State the blood parasite species.
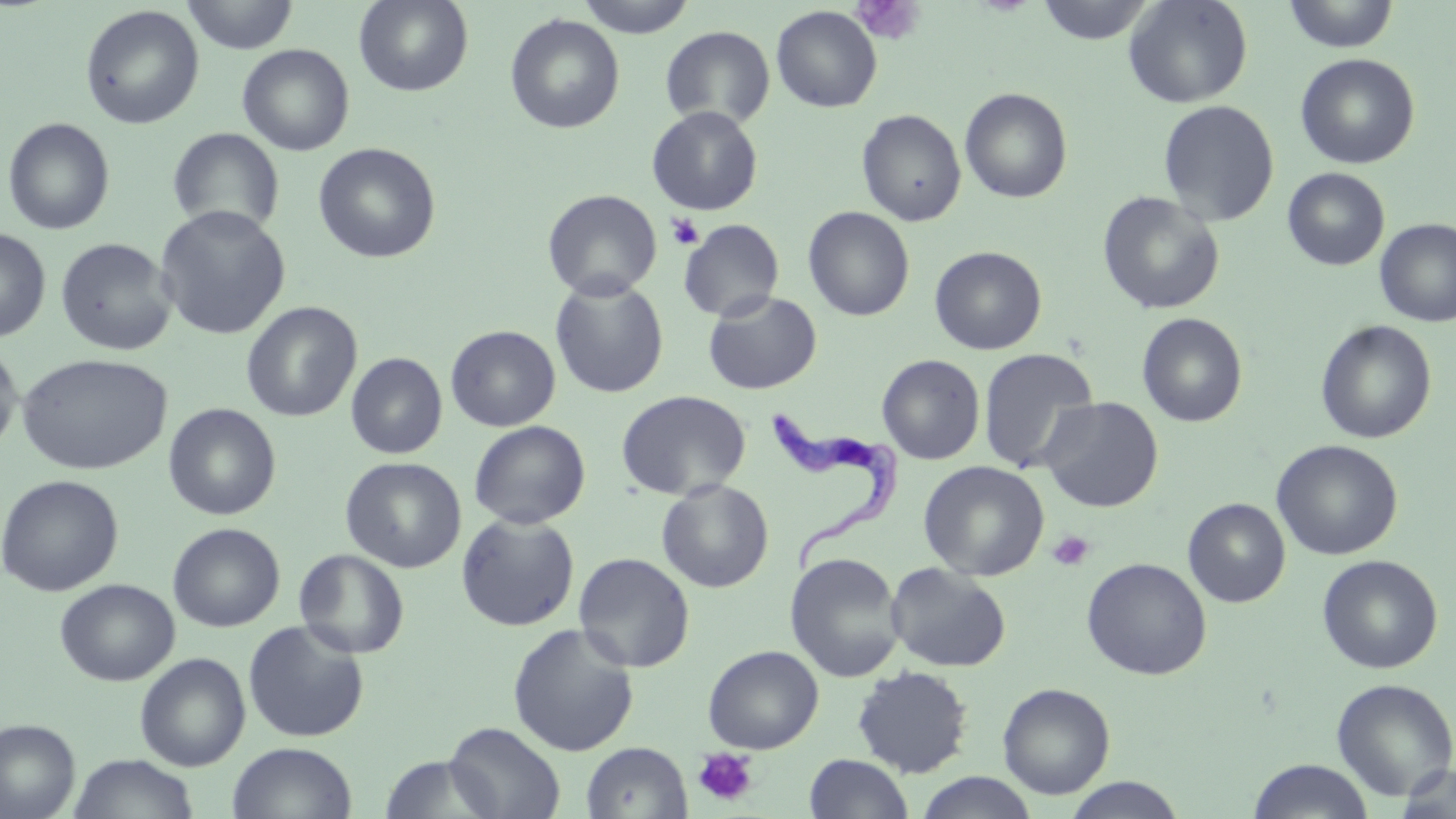

Trypanosoma brucei.

magnification = 1000x
stain = May-Grünwald-Giemsa
image size = 1456×819 pixels
modality = optical microscopy
preparation = thin blood film
Trypanosoma brucei locations = approximate bounding boxes as (x1,y1)-(x2,y2) corner pairs in pixels: (764,406)-(912,578)
field of view = one of a larger specimen
uninfected red blood cell locations = approximate bounding boxes as (x1,y1)-(x2,y2) corner pairs in pixels: (181,0)-(300,54), (354,0)-(473,96), (575,0)-(697,38), (1035,0)-(1158,44), (1123,0)-(1253,108), (1282,0)-(1400,52), (79,5)-(204,129), (771,6)-(882,112), (505,14)-(625,134), (660,25)-(775,129), (237,44)-(355,156), (1295,53)-(1420,169), (959,87)-(1073,203), (1157,99)-(1280,226), (647,106)-(763,215), (857,108)-(967,226), (3,117)-(115,235), (167,126)-(286,236), (313,142)-(441,264), (1283,168)-(1390,270), (543,189)-(662,300), (1097,191)-(1224,315), (154,205)-(291,340), (803,206)-(915,321), (678,218)-(785,321), (1374,218)-(1456,328), (0,228)-(51,343), (55,237)-(177,357), (929,246)-(1046,355), (550,277)-(669,398), (702,290)-(822,395), (241,301)-(362,422), (1136,312)-(1248,428), (1315,319)-(1437,444), (446,325)-(560,432), (0,345)-(24,457), (978,347)-(1099,473), (16,352)-(172,475), (346,352)-(448,459), (877,354)-(985,464), (616,389)-(751,501), (1039,396)-(1164,513), (163,403)-(281,520), (469,420)-(590,529), (1271,440)-(1403,560), (341,457)-(466,573), (918,460)-(1049,581), (0,474)-(123,597), (657,479)-(773,593), (1183,498)-(1291,607), (456,512)-(580,632), (167,522)-(285,632), (294,548)-(409,659), (785,551)-(905,683), (573,552)-(696,672), (1317,554)-(1443,674), (1081,557)-(1212,680), (885,562)-(1011,672), (55,578)-(180,686), (244,620)-(370,743), (507,623)-(639,756), (702,644)-(824,754), (135,653)-(250,770), (851,665)-(973,778), (1331,678)-(1456,801), (998,682)-(1115,799), (0,718)-(80,819), (444,721)-(566,819), (227,742)-(357,819), (581,742)-(692,819), (804,753)-(913,819), (67,754)-(200,818), (379,754)-(502,819), (1247,759)-(1375,819), (1393,763)-(1456,817), (915,772)-(1039,819), (1062,777)-(1187,818)
platelet locations = approximate bounding boxes as (x1,y1)-(x2,y2) corner pairs in pixels: (852,0)-(925,44), (666,212)-(705,250), (1048,531)-(1094,571), (693,747)-(759,807)